Locate every uninfected red blood cell.
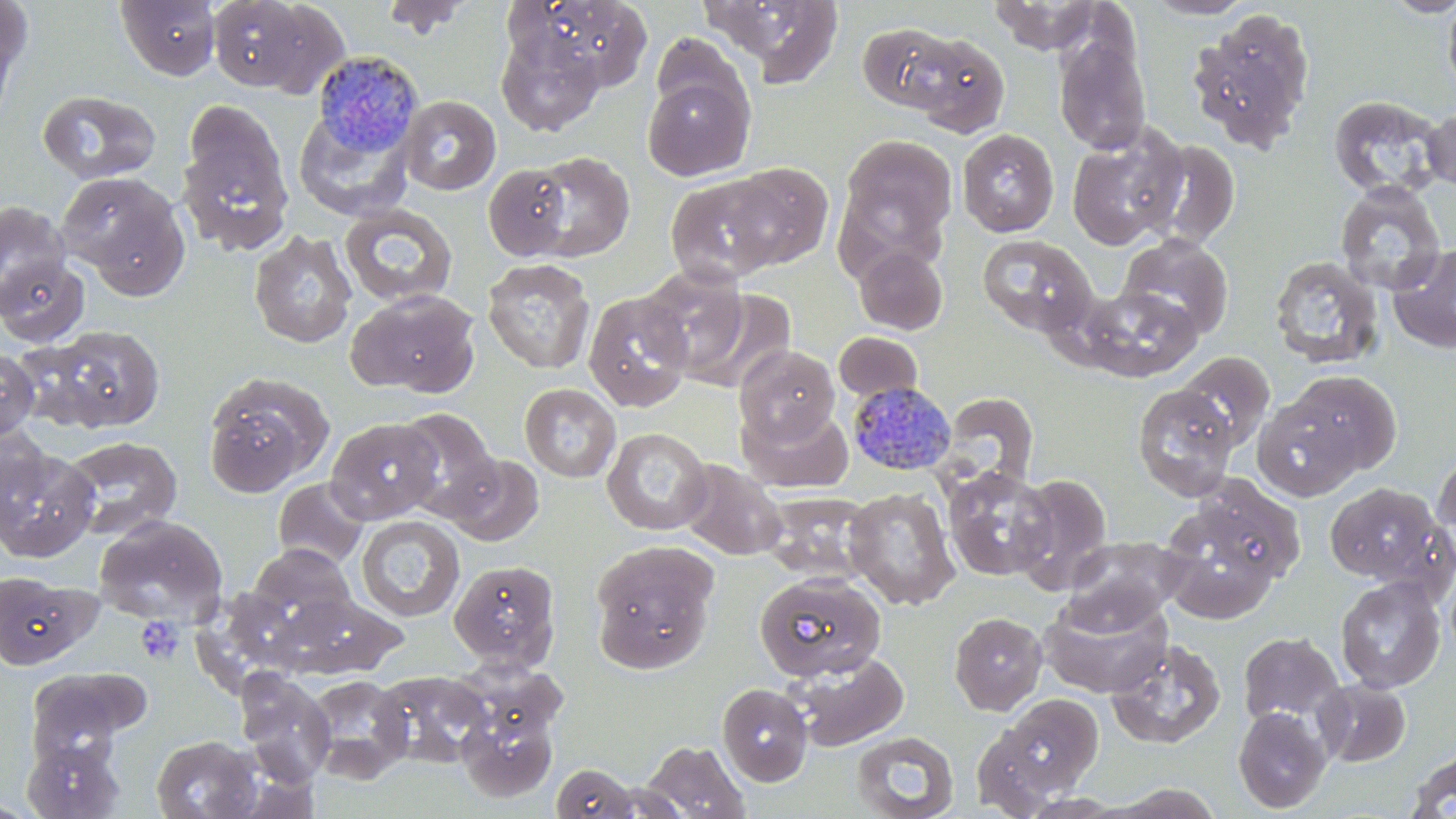

Approximate bounding boxes as (x1,y1)-(x2,y2) corner pairs in pixels.
Uninfected red blood cells: (0,0)-(34,81), (115,0)-(221,81), (206,0)-(336,93), (379,0)-(476,38), (530,0)-(654,91), (701,0)-(847,86), (1143,0)-(1256,20), (1382,0)-(1456,18), (988,1)-(1105,54), (1441,1)-(1456,103), (1187,9)-(1317,153), (1,11)-(22,137), (857,21)-(960,112), (495,29)-(605,137), (901,31)-(1010,138), (651,32)-(747,122), (1053,32)-(1152,155), (642,74)-(754,180), (36,90)-(163,184), (399,95)-(501,195), (1327,95)-(1446,199), (183,100)-(287,204), (1421,106)-(1455,192), (293,109)-(414,220), (1066,124)-(1188,251), (177,128)-(294,256), (956,128)-(1059,237), (838,134)-(958,257), (1146,140)-(1243,251), (527,151)-(635,261), (722,162)-(834,270), (483,163)-(574,261), (56,170)-(187,292), (665,176)-(782,287), (1334,182)-(1446,296), (0,201)-(71,316), (339,204)-(458,308), (248,230)-(357,350), (977,233)-(1099,337), (1117,234)-(1234,340), (1388,243)-(1456,355), (853,245)-(948,335), (1269,254)-(1385,370), (1,256)-(90,347), (482,258)-(596,374), (637,266)-(750,378), (1076,285)-(1202,381), (345,289)-(482,397), (683,289)-(796,393), (582,291)-(695,412), (41,326)-(167,432), (833,332)-(923,403), (735,345)-(839,445), (0,347)-(41,441), (1177,350)-(1275,452), (1285,370)-(1402,475), (202,372)-(334,496), (1132,382)-(1241,502), (519,383)-(621,483), (940,392)-(1040,487), (1253,396)-(1363,501), (739,404)-(853,492), (396,408)-(501,521), (327,420)-(444,522), (0,426)-(54,529), (602,427)-(712,535), (60,435)-(183,540), (1,445)-(101,562), (1432,450)-(1455,542), (443,452)-(545,546), (676,459)-(787,560), (942,465)-(1057,582), (1011,473)-(1112,591), (272,478)-(369,570), (1324,482)-(1450,588), (843,487)-(960,610), (761,492)-(874,583), (1157,497)-(1288,623), (91,513)-(229,625), (356,515)-(465,622), (1062,536)-(1191,631), (590,539)-(719,672), (246,543)-(357,631), (448,560)-(561,671), (1444,570)-(1456,666), (753,572)-(886,682), (0,573)-(92,669), (1334,575)-(1446,693), (277,592)-(406,679), (1038,593)-(1173,698), (949,612)-(1048,715), (1238,631)-(1345,725), (1105,637)-(1227,749), (786,651)-(909,751), (24,670)-(139,769), (374,670)-(494,769), (236,671)-(337,787), (303,675)-(413,784), (1314,678)-(1411,767), (717,682)-(812,786), (997,693)-(1104,798), (456,703)-(559,803), (1232,707)-(1331,813), (971,724)-(1062,817), (851,731)-(958,819), (150,735)-(264,819), (22,739)-(124,819), (640,740)-(751,819), (1404,748)-(1456,819), (551,763)-(641,819), (1109,783)-(1225,819).

slide_level_diagnosis: Plasmodium malariae
platelet_locations: 'approximate bounding boxes as (x1,y1)-(x2,y2) corner pairs in pixels: (135,615)-(185,665)'
magnification: 1000x
modality: optical microscopy
image_size: 1456×819 pixels
field_of_view: single
stain: May-Grünwald-Giemsa
preparation: thin blood smear
plasmodium_malariae_infected_red_blood_cell_locations: 'approximate bounding boxes as (x1,y1)-(x2,y2) corner pairs in pixels: (312,50)-(424,156), (847,382)-(956,476)'